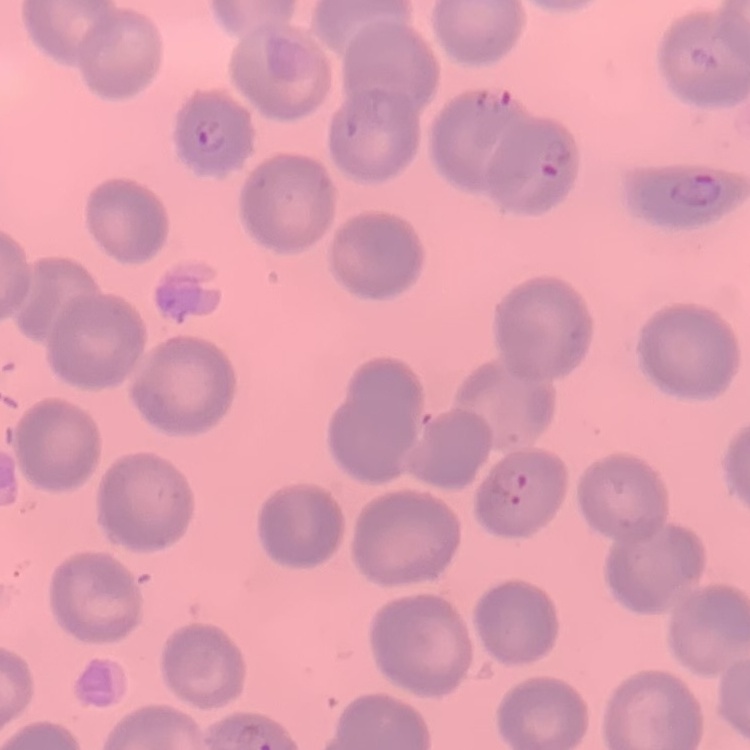

Summary:
  - Erythrocyte morphology: no rouleaux formation
  - Preparation: thin peripheral smear
  - Stain: Field's or Giemsa
  - Image type: one tile cut from a larger photomicrograph